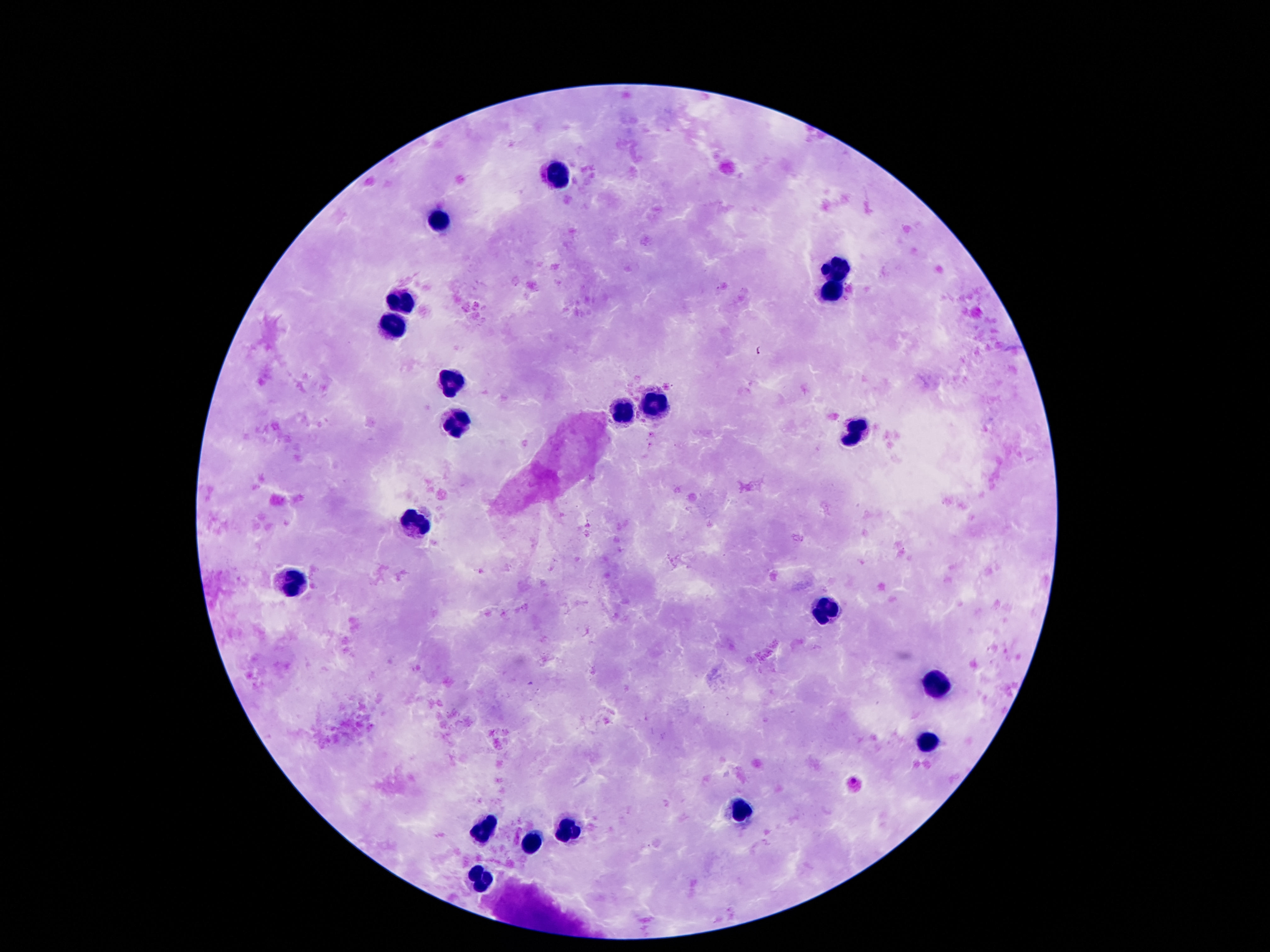
{
  "field_of_view": "single",
  "capture": "smartphone camera through the microscope eyepiece",
  "stain": "Giemsa",
  "image_size": "1270×952 pixels",
  "leukocyte_locations": "approximate centers as {x, y} in pixels: {557, 175}, {437, 223}, {836, 269}, {829, 294}, {400, 304}, {392, 324}, {453, 386}, {657, 408}, {621, 413}, {456, 424}, {854, 434}, {414, 527}, {291, 582}, {824, 610}, {936, 684}, {930, 743}, {738, 808}, {484, 829}, {568, 829}, {533, 842}, {481, 878}",
  "preparation": "thick blood smear",
  "patient_malaria_status": "not infected",
  "magnification": "100x"
}